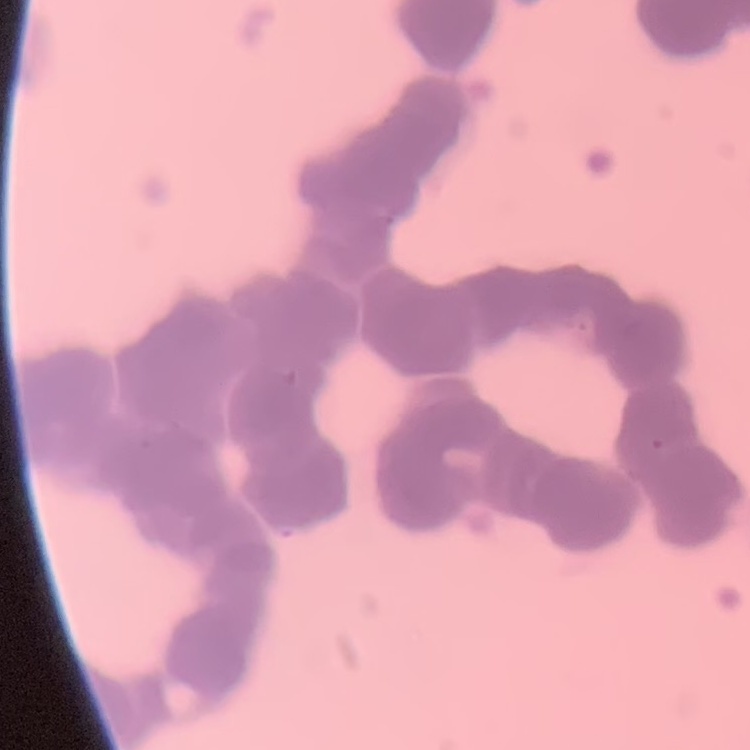

erythrocyte morphology = rouleaux formation
preparation = thin blood film
image type = one tile cut from a larger photomicrograph
stain = Field's or Giemsa